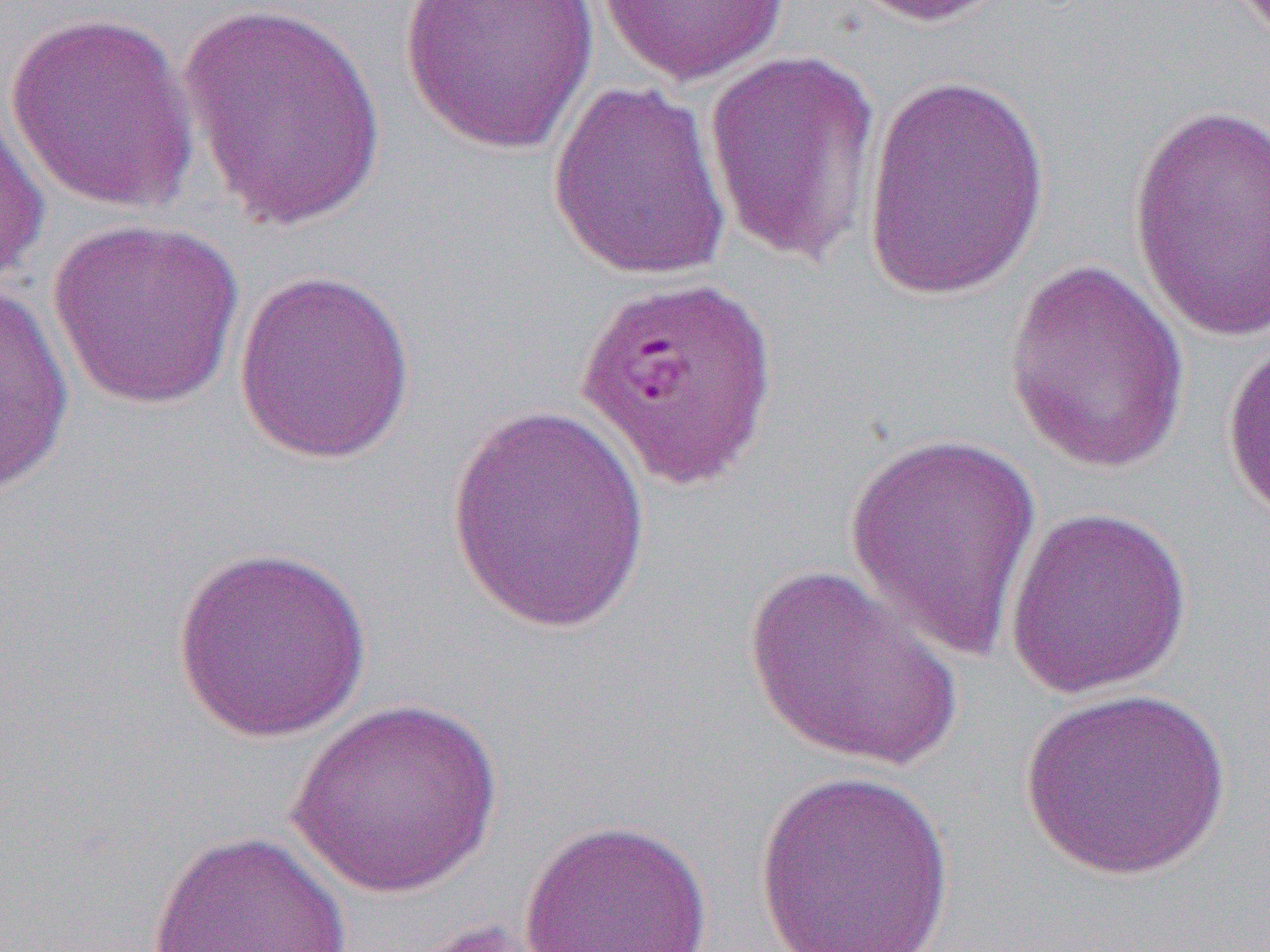

slide-level diagnosis = Plasmodium falciparum
modality = light microscopy
magnification = 1000x
image size = 1270×952 pixels
preparation = thin blood film
field of view = one of a larger specimen
uninfected red blood cell locations = approximate bounding boxes as named x1/y1/x2/y2 corners in pixels: (x1=399, y1=0, x2=599, y2=156), (x1=596, y1=0, x2=791, y2=86), (x1=845, y1=0, x2=1018, y2=27), (x1=175, y1=1, x2=388, y2=231), (x1=4, y1=9, x2=201, y2=213), (x1=703, y1=47, x2=883, y2=268), (x1=861, y1=72, x2=1053, y2=303), (x1=547, y1=81, x2=733, y2=282), (x1=0, y1=104, x2=49, y2=290), (x1=1128, y1=104, x2=1269, y2=343), (x1=48, y1=217, x2=246, y2=410), (x1=1003, y1=257, x2=1193, y2=474), (x1=232, y1=267, x2=417, y2=465), (x1=0, y1=284, x2=75, y2=498), (x1=1221, y1=334, x2=1270, y2=524), (x1=444, y1=401, x2=651, y2=636), (x1=842, y1=430, x2=1046, y2=663), (x1=1005, y1=504, x2=1193, y2=699), (x1=171, y1=546, x2=373, y2=741), (x1=743, y1=562, x2=963, y2=774), (x1=1018, y1=687, x2=1232, y2=882), (x1=285, y1=699, x2=505, y2=899), (x1=755, y1=769, x2=955, y2=951), (x1=518, y1=818, x2=715, y2=952), (x1=144, y1=829, x2=357, y2=952)